Assess this cell for malaria.
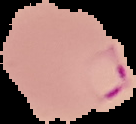
It is parasitized.

Segmented cell region on a black background. Image is 136×124 pixels. From a thin blood film.